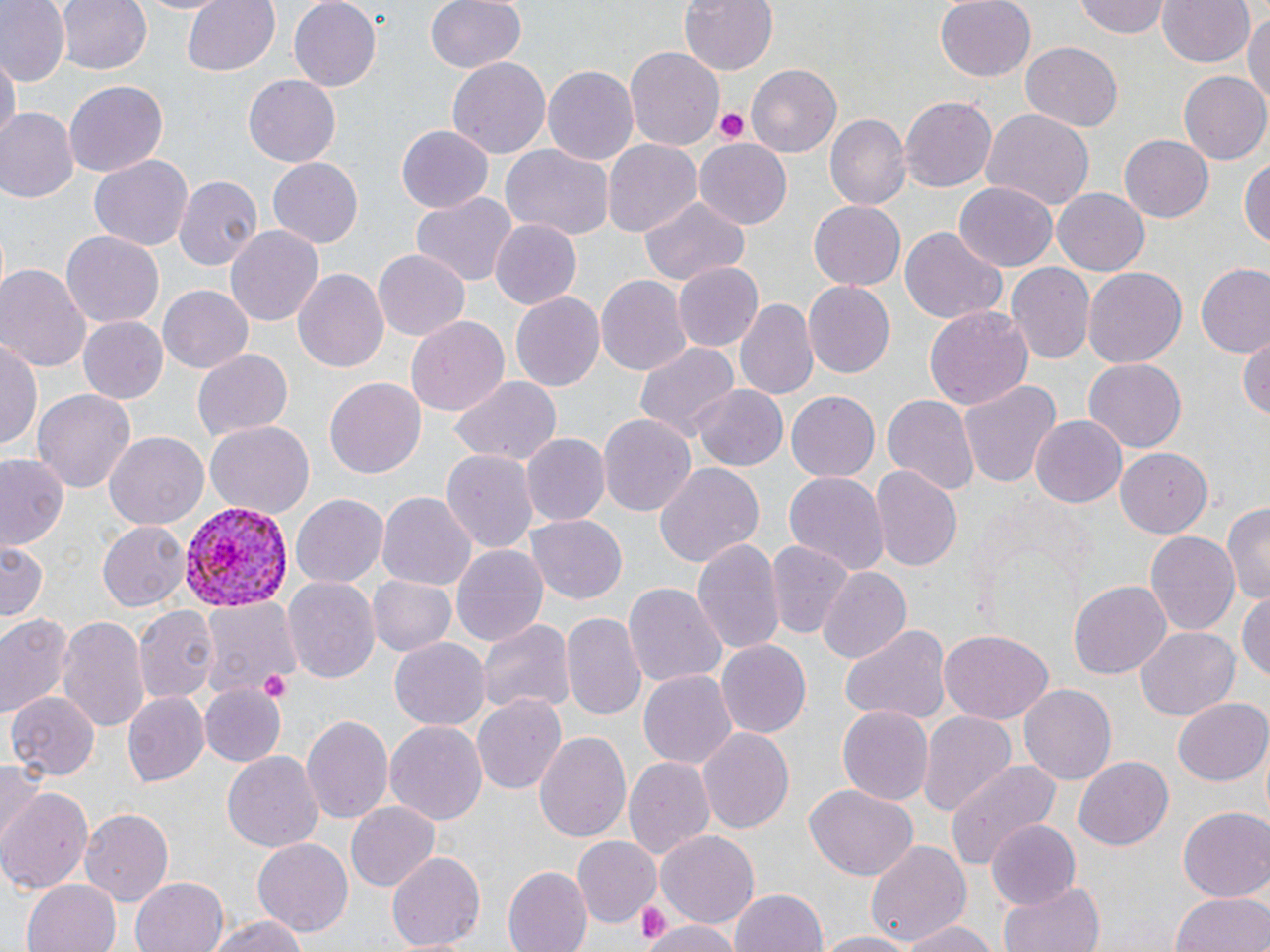

Approximate bounding boxes as named x1/y1/x2/y2 corners in pixels. Uninfected red blood cell locations: (x1=0, y1=0, x2=69, y2=85), (x1=57, y1=0, x2=151, y2=76), (x1=130, y1=0, x2=230, y2=16), (x1=182, y1=0, x2=280, y2=76), (x1=288, y1=0, x2=382, y2=91), (x1=424, y1=0, x2=527, y2=75), (x1=677, y1=0, x2=778, y2=76), (x1=933, y1=0, x2=1037, y2=84), (x1=1073, y1=0, x2=1171, y2=39), (x1=1157, y1=0, x2=1256, y2=69), (x1=1244, y1=8, x2=1270, y2=115), (x1=1021, y1=42, x2=1122, y2=131), (x1=624, y1=47, x2=724, y2=150), (x1=2, y1=52, x2=18, y2=151), (x1=448, y1=57, x2=550, y2=161), (x1=542, y1=64, x2=640, y2=166), (x1=746, y1=64, x2=842, y2=157), (x1=1179, y1=71, x2=1268, y2=166), (x1=243, y1=76, x2=340, y2=167), (x1=65, y1=81, x2=169, y2=176), (x1=899, y1=96, x2=997, y2=193), (x1=0, y1=108, x2=77, y2=203), (x1=981, y1=108, x2=1094, y2=210), (x1=826, y1=114, x2=910, y2=211), (x1=396, y1=125, x2=494, y2=214), (x1=1119, y1=136, x2=1212, y2=222), (x1=694, y1=137, x2=793, y2=229), (x1=604, y1=139, x2=703, y2=237), (x1=502, y1=147, x2=615, y2=240), (x1=1240, y1=152, x2=1269, y2=253), (x1=88, y1=155, x2=194, y2=252), (x1=266, y1=159, x2=365, y2=248), (x1=174, y1=173, x2=261, y2=270), (x1=955, y1=182, x2=1058, y2=270), (x1=1052, y1=188, x2=1150, y2=277), (x1=411, y1=193, x2=516, y2=287), (x1=636, y1=197, x2=751, y2=286), (x1=808, y1=198, x2=909, y2=289), (x1=489, y1=219, x2=582, y2=310), (x1=225, y1=223, x2=323, y2=328), (x1=899, y1=226, x2=1007, y2=323), (x1=62, y1=231, x2=164, y2=327), (x1=372, y1=250, x2=469, y2=339), (x1=0, y1=262, x2=91, y2=374), (x1=674, y1=262, x2=763, y2=352), (x1=1007, y1=263, x2=1095, y2=364), (x1=1083, y1=264, x2=1186, y2=365), (x1=1196, y1=266, x2=1270, y2=359), (x1=293, y1=267, x2=388, y2=372), (x1=596, y1=274, x2=691, y2=377), (x1=802, y1=282, x2=895, y2=379), (x1=155, y1=285, x2=254, y2=373), (x1=512, y1=291, x2=605, y2=392), (x1=735, y1=296, x2=817, y2=403), (x1=923, y1=306, x2=1034, y2=415), (x1=77, y1=316, x2=169, y2=404), (x1=406, y1=316, x2=508, y2=415), (x1=1, y1=333, x2=42, y2=457), (x1=1238, y1=334, x2=1270, y2=423), (x1=633, y1=340, x2=739, y2=447), (x1=193, y1=349, x2=293, y2=442), (x1=1081, y1=360, x2=1186, y2=452), (x1=324, y1=375, x2=425, y2=476), (x1=448, y1=376, x2=561, y2=468), (x1=958, y1=380, x2=1062, y2=491), (x1=692, y1=382, x2=787, y2=469), (x1=35, y1=387, x2=136, y2=496), (x1=787, y1=391, x2=879, y2=480), (x1=882, y1=392, x2=977, y2=495), (x1=598, y1=414, x2=695, y2=518), (x1=1030, y1=416, x2=1126, y2=506), (x1=204, y1=422, x2=314, y2=519), (x1=104, y1=431, x2=209, y2=529), (x1=520, y1=434, x2=609, y2=527), (x1=443, y1=449, x2=538, y2=556), (x1=1115, y1=450, x2=1213, y2=537), (x1=0, y1=451, x2=68, y2=551), (x1=653, y1=461, x2=764, y2=572), (x1=869, y1=465, x2=963, y2=575), (x1=781, y1=468, x2=888, y2=574), (x1=378, y1=492, x2=476, y2=591), (x1=292, y1=493, x2=388, y2=588), (x1=1223, y1=500, x2=1270, y2=606), (x1=525, y1=514, x2=627, y2=604), (x1=99, y1=521, x2=189, y2=612), (x1=1146, y1=530, x2=1240, y2=639), (x1=692, y1=536, x2=786, y2=659), (x1=764, y1=538, x2=853, y2=640), (x1=0, y1=540, x2=47, y2=625), (x1=451, y1=544, x2=548, y2=651), (x1=818, y1=567, x2=911, y2=666), (x1=283, y1=575, x2=379, y2=688), (x1=369, y1=576, x2=455, y2=657), (x1=1070, y1=578, x2=1174, y2=679), (x1=622, y1=579, x2=726, y2=687), (x1=1237, y1=589, x2=1270, y2=687), (x1=199, y1=600, x2=298, y2=703), (x1=136, y1=604, x2=218, y2=704), (x1=561, y1=610, x2=646, y2=721), (x1=0, y1=611, x2=73, y2=719), (x1=58, y1=613, x2=151, y2=734), (x1=474, y1=615, x2=576, y2=718), (x1=838, y1=623, x2=951, y2=727), (x1=1134, y1=626, x2=1241, y2=720), (x1=937, y1=631, x2=1051, y2=725), (x1=388, y1=635, x2=489, y2=729), (x1=716, y1=640, x2=811, y2=739), (x1=638, y1=668, x2=737, y2=769), (x1=200, y1=684, x2=285, y2=764), (x1=1021, y1=684, x2=1116, y2=784), (x1=9, y1=689, x2=99, y2=779), (x1=122, y1=691, x2=210, y2=789), (x1=472, y1=693, x2=566, y2=796), (x1=1172, y1=699, x2=1270, y2=786), (x1=835, y1=704, x2=935, y2=806), (x1=918, y1=711, x2=1017, y2=817), (x1=301, y1=713, x2=394, y2=824), (x1=384, y1=721, x2=488, y2=827), (x1=697, y1=726, x2=794, y2=834), (x1=534, y1=730, x2=632, y2=847), (x1=223, y1=750, x2=323, y2=852), (x1=624, y1=754, x2=713, y2=862), (x1=1073, y1=756, x2=1172, y2=852), (x1=0, y1=757, x2=46, y2=843), (x1=946, y1=757, x2=1062, y2=870), (x1=805, y1=784, x2=917, y2=881), (x1=0, y1=787, x2=91, y2=893), (x1=346, y1=803, x2=440, y2=894), (x1=1178, y1=805, x2=1270, y2=902), (x1=79, y1=807, x2=174, y2=904), (x1=987, y1=820, x2=1083, y2=911), (x1=656, y1=831, x2=759, y2=927), (x1=573, y1=836, x2=660, y2=928), (x1=251, y1=838, x2=354, y2=936), (x1=865, y1=840, x2=972, y2=948), (x1=386, y1=850, x2=485, y2=952), (x1=503, y1=866, x2=591, y2=952), (x1=130, y1=876, x2=230, y2=952), (x1=22, y1=879, x2=119, y2=952), (x1=1000, y1=879, x2=1105, y2=952), (x1=730, y1=888, x2=827, y2=952), (x1=1171, y1=892, x2=1270, y2=952), (x1=202, y1=913, x2=318, y2=952), (x1=648, y1=918, x2=737, y2=952), (x1=897, y1=918, x2=1001, y2=952), (x1=812, y1=930, x2=924, y2=952). Plasmodium vivax-infected red blood cell locations: (x1=178, y1=500, x2=291, y2=613). Platelet locations: (x1=716, y1=109, x2=750, y2=144), (x1=257, y1=668, x2=293, y2=701), (x1=636, y1=905, x2=667, y2=945). Slide-level diagnosis: Plasmodium vivax. Single field of view. Image is 1270×952 pixels. May-Grünwald-Giemsa-stained preparation. Thin blood smear. Light microscopy. Captured at 1000x magnification.